Classify this cell by malaria status.
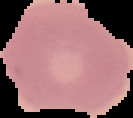

Uninfected.

image type = cell region segmented out of the field of view; surrounding area masked to black
image size = 133×118 pixels
preparation = thin blood smear